Outline each blood parasite and name the species.
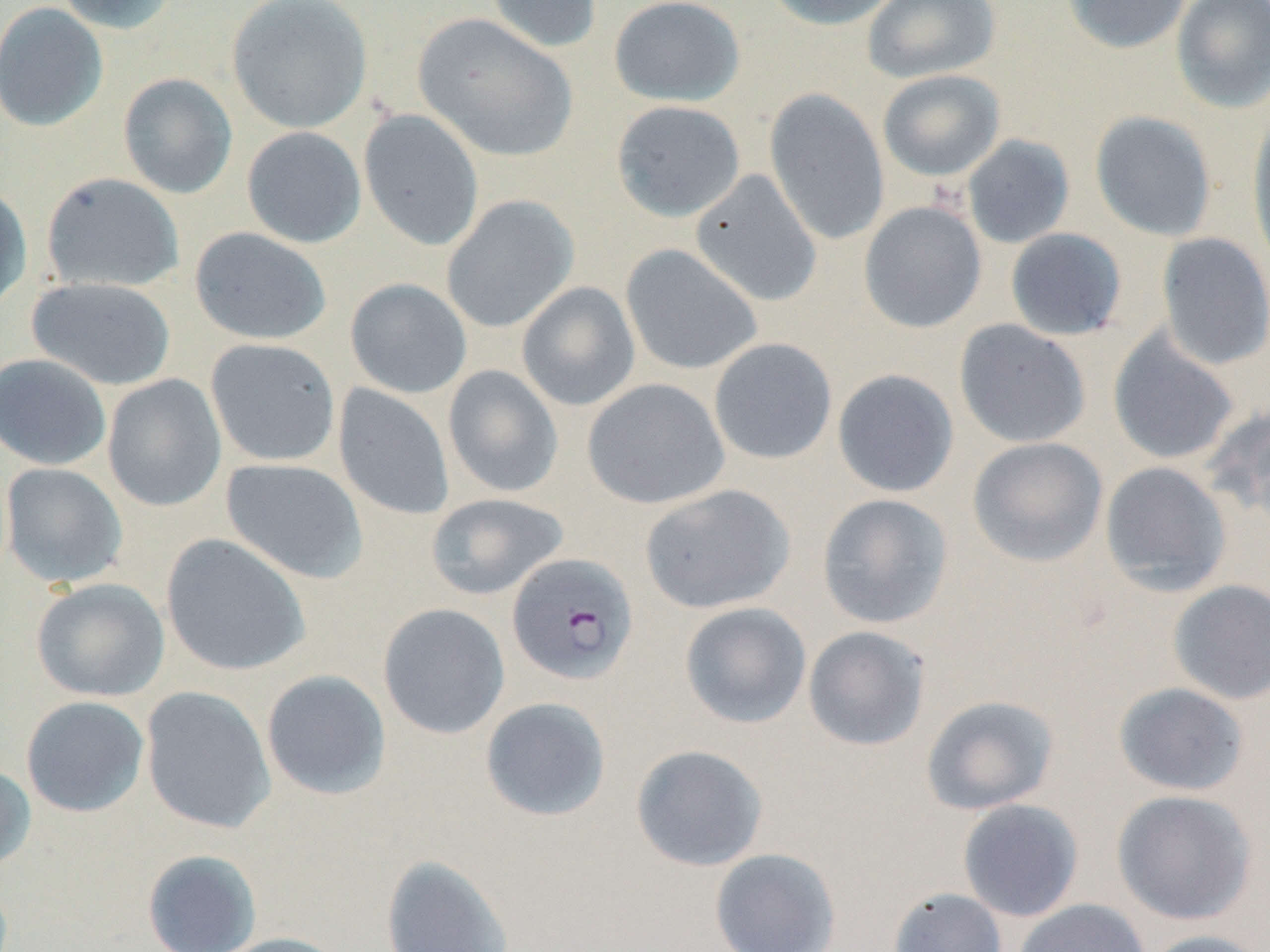
Approximate bounding boxes as (x1,y1)-(x2,y2) corner pairs in pixels.
Plasmodium falciparum-infected red blood cells: (506,552)-(639,686).
No Plasmodium ovale, Plasmodium malariae, Plasmodium vivax, Babesia divergens, or Trypanosoma brucei observed.

Summary:
  - Uninfected red blood cell locations: (53,0)-(182,35), (226,0)-(373,133), (484,0)-(602,54), (608,0)-(745,107), (763,0)-(905,30), (863,0)-(1001,83), (1062,0)-(1192,54), (1171,0)-(1270,114), (0,2)-(108,132), (413,13)-(578,163), (877,70)-(1005,181), (118,73)-(238,199), (763,87)-(891,246), (611,100)-(745,222), (358,109)-(484,251), (1089,111)-(1217,241), (1246,116)-(1270,272), (241,126)-(367,248), (962,134)-(1075,249), (690,169)-(822,307), (41,172)-(186,294), (0,183)-(32,315), (441,195)-(579,334), (858,201)-(987,334), (190,227)-(331,345), (1004,227)-(1128,341), (1156,232)-(1270,371), (620,244)-(763,376), (26,277)-(177,391), (344,278)-(472,399), (516,282)-(641,411), (953,319)-(1091,448), (1108,328)-(1240,466), (708,337)-(838,465), (205,338)-(341,467), (0,353)-(112,471), (442,365)-(564,499), (832,369)-(959,497), (102,374)-(226,512), (581,378)-(730,509), (333,384)-(455,521), (1203,403)-(1270,527), (967,437)-(1108,568), (221,458)-(368,583), (1099,461)-(1232,597), (0,463)-(128,589), (639,483)-(796,614), (425,492)-(570,601), (816,493)-(954,629), (160,533)-(310,677), (30,578)-(169,702), (1167,580)-(1270,704), (679,602)-(812,729), (378,603)-(510,739), (802,625)-(931,752), (261,669)-(392,800), (1113,682)-(1249,796), (140,686)-(276,834), (920,694)-(1060,815), (20,696)-(149,817), (479,696)-(611,822), (630,744)-(769,872), (0,763)-(36,873), (1112,789)-(1257,926), (957,799)-(1084,922), (709,847)-(842,952), (141,849)-(262,952), (380,854)-(515,952), (888,886)-(1008,952), (1013,899)-(1151,952), (1139,930)-(1270,952), (210,932)-(353,952)
  - Slide-level diagnosis: Plasmodium falciparum
  - Image size: 1270×952 pixels
  - Preparation: thin blood smear
  - Stain: May-Grünwald-Giemsa
  - Field of view: single
  - Modality: optical microscopy
  - Magnification: 1000x